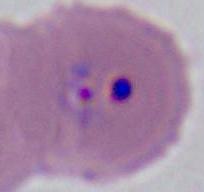
identification = Plasmodium
modality = micrograph
magnification = 400x or 1000x